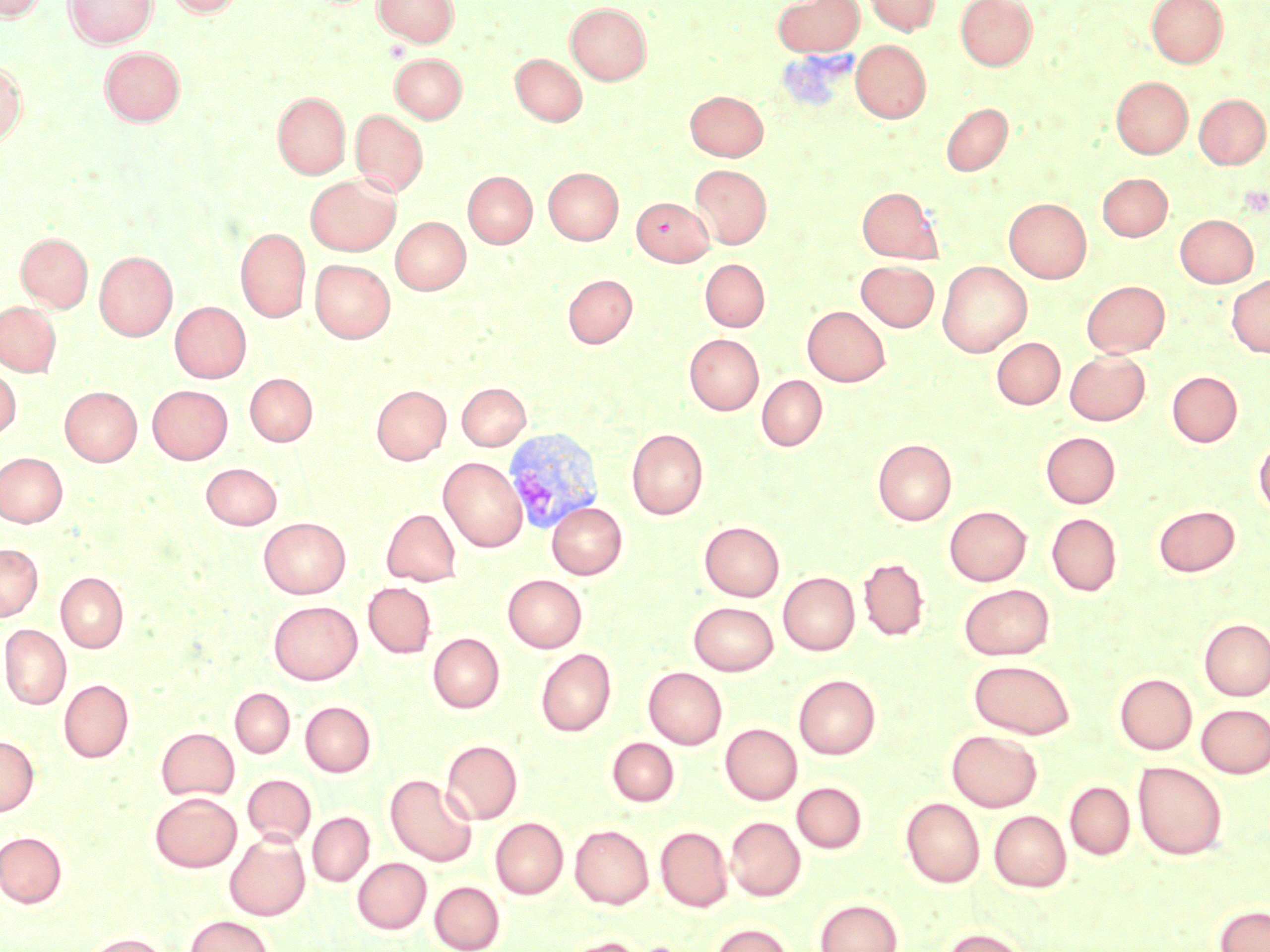

{
  "slide_level_diagnosis": "Plasmodium vivax",
  "uninfected_red_blood_cell_locations": "approximate bounding boxes as (x1, y1, x2, y2) in pixels: (0, 0, 46, 22), (64, 0, 158, 48), (165, 0, 244, 17), (374, 0, 460, 46), (772, 0, 864, 56), (864, 0, 939, 35), (955, 0, 1037, 70), (1146, 0, 1228, 68), (565, 3, 651, 85), (851, 40, 930, 122), (100, 46, 185, 125), (390, 53, 467, 123), (511, 53, 587, 126), (0, 60, 26, 145), (1111, 76, 1193, 158), (685, 90, 768, 160), (273, 92, 350, 178), (1195, 94, 1269, 169), (941, 102, 1012, 176), (351, 109, 428, 197), (689, 165, 772, 249), (544, 167, 623, 244), (463, 171, 537, 248), (1098, 173, 1172, 241), (305, 174, 400, 255), (857, 187, 942, 263), (631, 197, 713, 265), (1004, 198, 1091, 283), (1175, 214, 1258, 287), (392, 217, 470, 294), (236, 228, 310, 322), (16, 232, 92, 311), (95, 251, 177, 340), (310, 259, 395, 342), (700, 259, 769, 332), (856, 260, 939, 331), (937, 261, 1032, 357), (563, 274, 637, 348), (1227, 275, 1270, 357), (1083, 280, 1169, 357), (0, 301, 60, 375), (170, 301, 251, 382), (803, 306, 890, 386), (685, 334, 764, 415), (991, 337, 1065, 409), (1065, 350, 1149, 425), (0, 365, 20, 440), (1167, 372, 1242, 447), (245, 373, 317, 445), (757, 375, 827, 451), (457, 382, 530, 450), (147, 385, 233, 464), (372, 385, 450, 464), (60, 386, 141, 465), (627, 428, 708, 519), (1041, 432, 1120, 508), (1254, 438, 1270, 517), (873, 439, 957, 526), (0, 452, 67, 527), (439, 457, 527, 551), (201, 463, 282, 530), (547, 502, 627, 579), (1153, 505, 1240, 576), (945, 506, 1030, 585), (954, 506, 1040, 659), (382, 509, 460, 586), (1046, 513, 1122, 596), (259, 517, 350, 599), (699, 521, 784, 601), (0, 543, 42, 621), (859, 557, 929, 641), (56, 572, 128, 652), (778, 572, 860, 655), (503, 574, 587, 652), (363, 582, 436, 658), (959, 583, 1054, 660), (268, 600, 362, 684), (689, 602, 778, 675), (1199, 618, 1270, 700), (0, 624, 71, 710), (428, 633, 504, 713), (535, 648, 616, 737), (969, 659, 1076, 738), (644, 667, 727, 749), (1115, 673, 1197, 754), (793, 675, 880, 759), (59, 679, 133, 762), (230, 688, 294, 758), (300, 701, 376, 776), (1197, 704, 1270, 778), (720, 723, 802, 804), (156, 727, 239, 800), (947, 729, 1042, 811), (0, 735, 39, 816), (607, 737, 679, 806), (442, 739, 522, 824), (1133, 761, 1227, 860), (242, 774, 316, 846), (385, 775, 477, 867), (792, 782, 867, 853), (1065, 782, 1135, 859), (150, 792, 241, 872), (901, 797, 985, 887), (989, 810, 1071, 891), (308, 812, 374, 886), (726, 817, 805, 901), (490, 818, 568, 898), (570, 824, 654, 908), (656, 826, 733, 911), (0, 831, 67, 907), (225, 832, 310, 920), (352, 858, 431, 934), (430, 881, 505, 952), (815, 898, 903, 952), (1215, 905, 1270, 952), (185, 915, 274, 952), (707, 923, 796, 952), (941, 927, 1031, 952), (84, 933, 167, 952), (561, 937, 645, 952)",
  "plasmodium_vivax_infected_red_blood_cell_locations": "approximate bounding boxes as (x1, y1, x2, y2) in pixels: (504, 427, 605, 535)",
  "modality": "optical microscopy",
  "preparation": "thin blood film",
  "magnification": "1000x",
  "image_size": "1270×952 pixels",
  "field_of_view": "one of a larger specimen",
  "stain": "May-Grünwald-Giemsa"
}